Assess this cell for malaria.
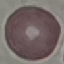
Uninfected.

Summary:
  - Preparation: thin smear
  - Stain: Giemsa
  - Image type: automatically extracted cell patch, resized to 64 × 64 pixels
  - Capture: smartphone camera at the microscope eyepiece